Assess the morphology of the red blood cells.
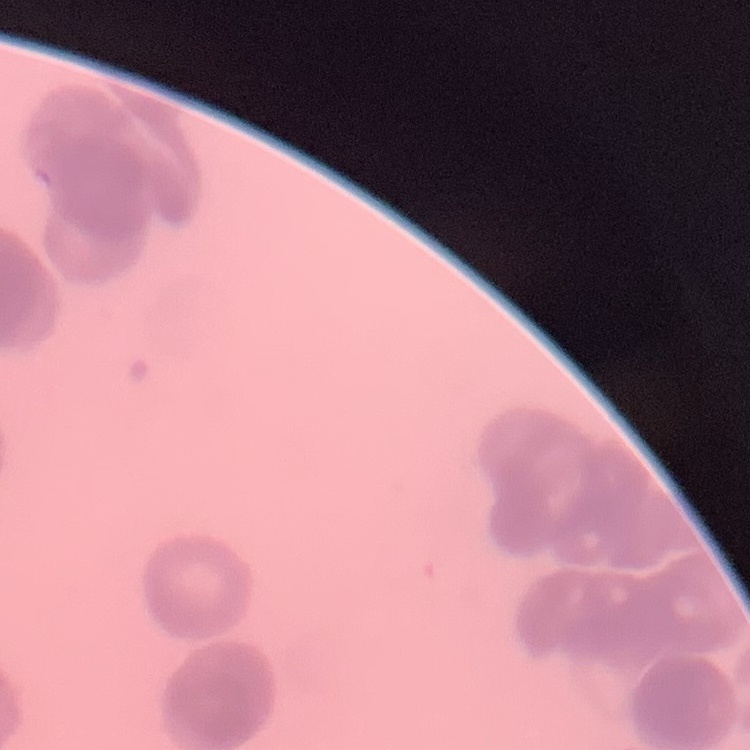

Rouleaux formation.

Thin blood smear. Stained with either Field's or Giemsa. Square crop of a larger photomicrograph.